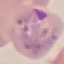

Summary:
  - Result: malaria parasites detected
  - Stain: Giemsa
  - Image type: automatically extracted cell patch, resized to 64 × 64 pixels
  - Capture: smartphone camera at the microscope eyepiece
  - Preparation: thin smear